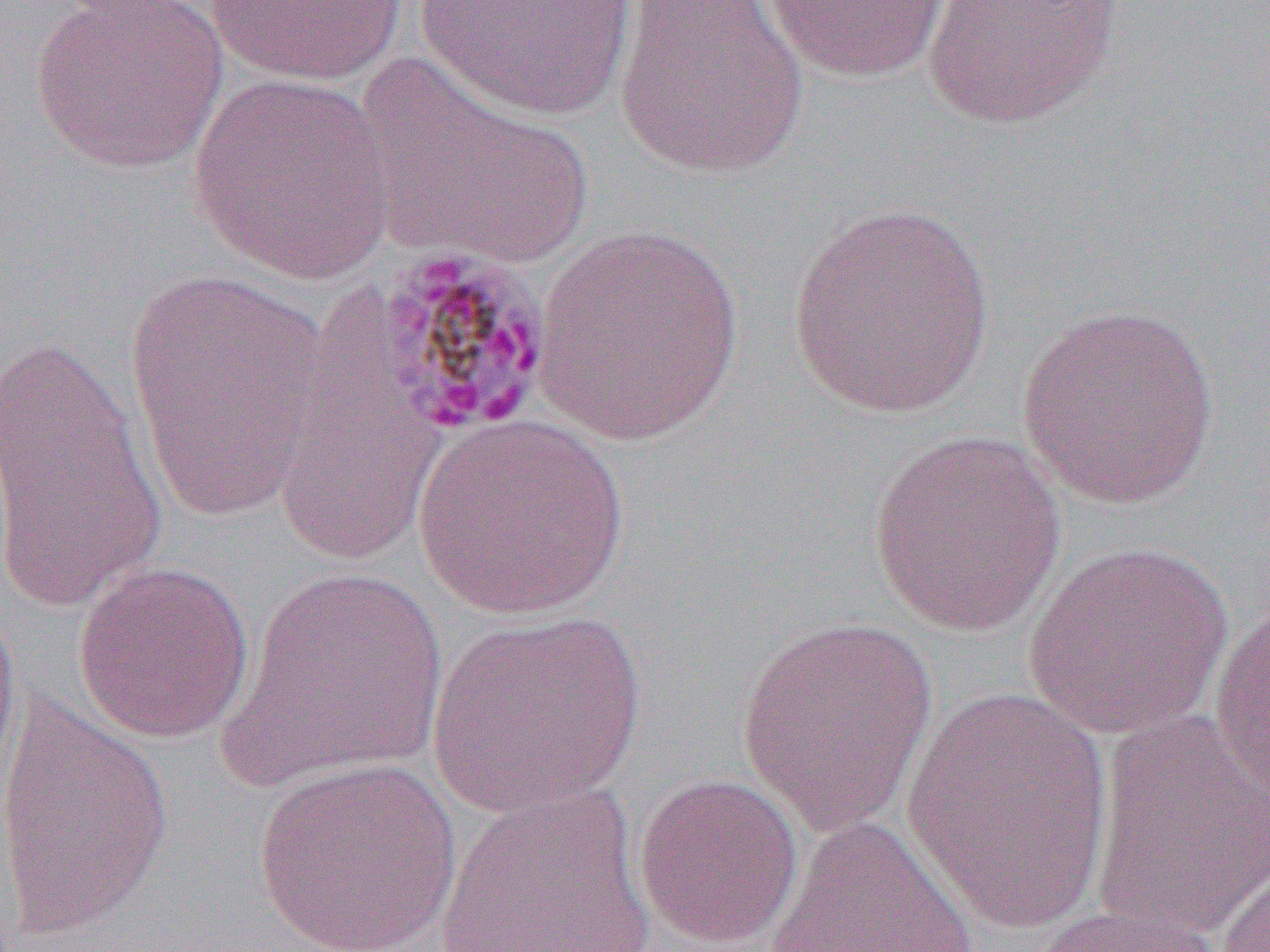

{
  "slide_level_diagnosis": "Plasmodium malariae",
  "uninfected_red_blood_cell_locations": "approximate bounding boxes as named x1/y1/x2/y2 corners in pixels: (x1=205, y1=0, x2=408, y2=86), (x1=414, y1=0, x2=637, y2=121), (x1=613, y1=0, x2=809, y2=180), (x1=761, y1=0, x2=954, y2=83), (x1=922, y1=0, x2=1122, y2=129), (x1=30, y1=1, x2=231, y2=175), (x1=352, y1=54, x2=597, y2=271), (x1=186, y1=72, x2=400, y2=284), (x1=786, y1=200, x2=1000, y2=419), (x1=529, y1=223, x2=750, y2=447), (x1=122, y1=266, x2=333, y2=523), (x1=1016, y1=303, x2=1223, y2=510), (x1=0, y1=332, x2=167, y2=619), (x1=267, y1=359, x2=445, y2=571), (x1=410, y1=414, x2=631, y2=620), (x1=868, y1=431, x2=1067, y2=638), (x1=1020, y1=540, x2=1235, y2=741), (x1=73, y1=559, x2=255, y2=744), (x1=219, y1=566, x2=448, y2=792), (x1=1207, y1=591, x2=1270, y2=812), (x1=0, y1=592, x2=21, y2=793), (x1=426, y1=610, x2=646, y2=816), (x1=735, y1=616, x2=939, y2=836), (x1=899, y1=687, x2=1117, y2=934), (x1=0, y1=688, x2=175, y2=944), (x1=1089, y1=708, x2=1269, y2=942), (x1=251, y1=756, x2=464, y2=951), (x1=633, y1=772, x2=804, y2=950), (x1=434, y1=780, x2=656, y2=952), (x1=762, y1=815, x2=979, y2=952), (x1=1215, y1=856, x2=1270, y2=952), (x1=1027, y1=900, x2=1228, y2=952)",
  "image_size": "1270×952 pixels",
  "field_of_view": "one of a larger specimen",
  "magnification": "1000x",
  "preparation": "thin blood smear",
  "modality": "light microscopy",
  "plasmodium_malariae_infected_red_blood_cell_locations": "approximate bounding boxes as named x1/y1/x2/y2 corners in pixels: (x1=374, y1=245, x2=556, y2=438)"
}